Describe the morphology of the red blood cells.
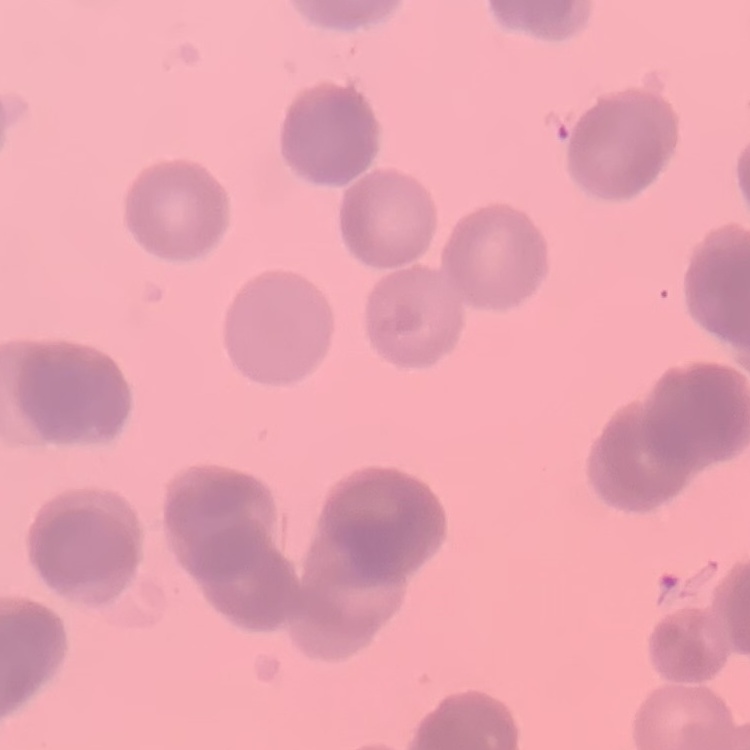

They show rouleaux formation.

Summary:
  - Image type: square crop of a larger photomicrograph
  - Stain: Field's or Giemsa
  - Preparation: thin blood film